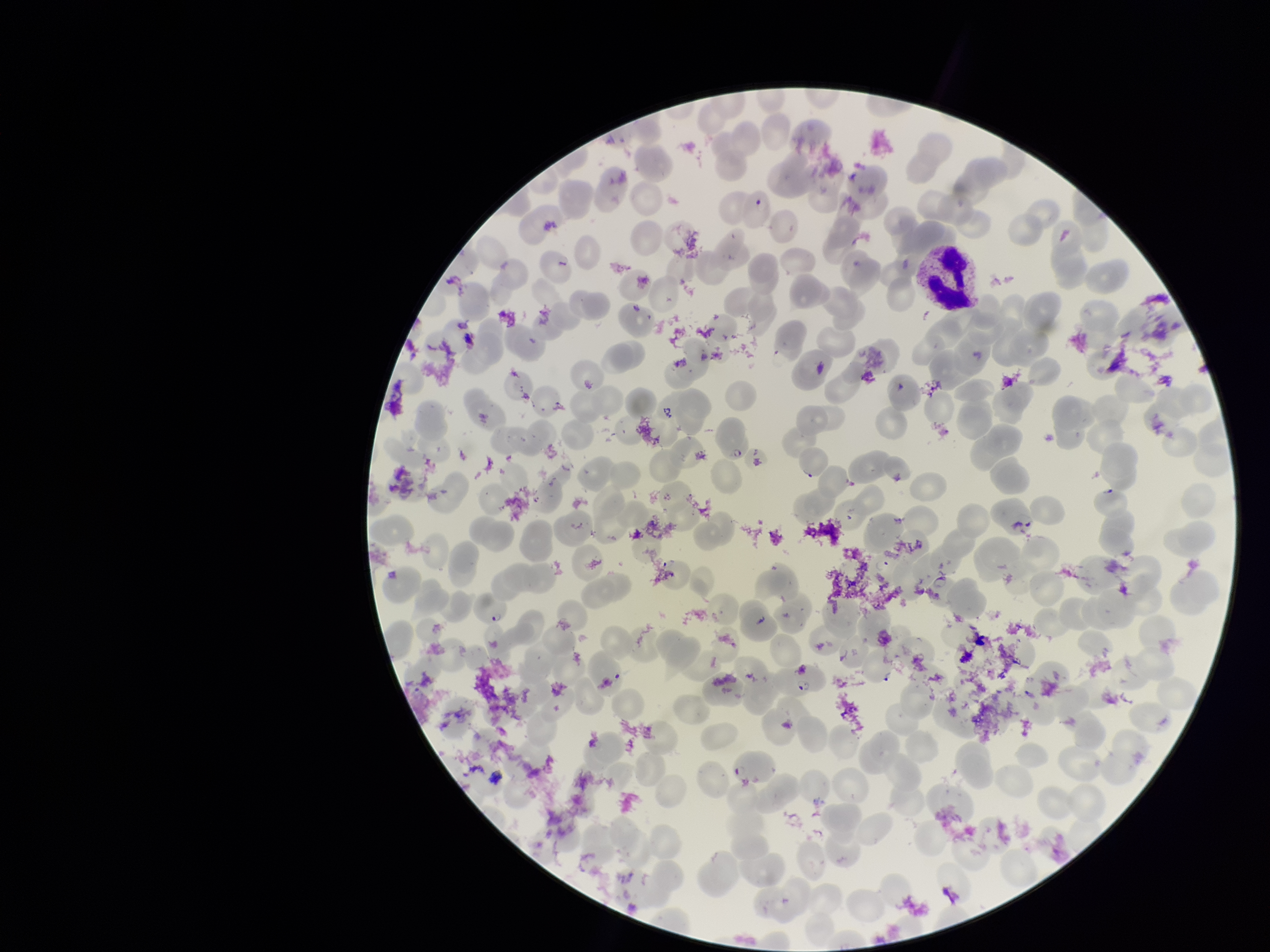
Red blood cell count: 263. Patient malaria status: positive. Single field of view. Species reported for this patient: Plasmodium falciparum. Image is 1270×952 pixels. Parasitized red blood cells: detected. Parasitized red blood cell count: 4. Preparation: thin smear. Photographed through the microscope eyepiece with a smartphone camera. Stained with Giemsa.